Describe the morphology of the erythrocytes.
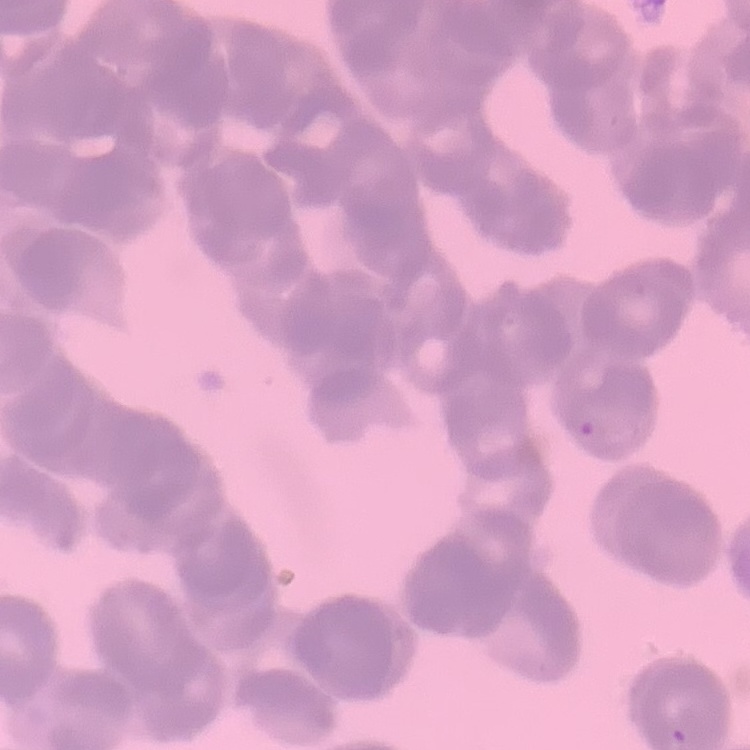

They show rouleaux formation.

Thin blood film. Field's or Giemsa stain. One tile cut from a larger photomicrograph.